Identify the parasite.
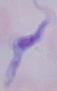
This is a trypanosome.

magnification = 1000x
modality = micrograph